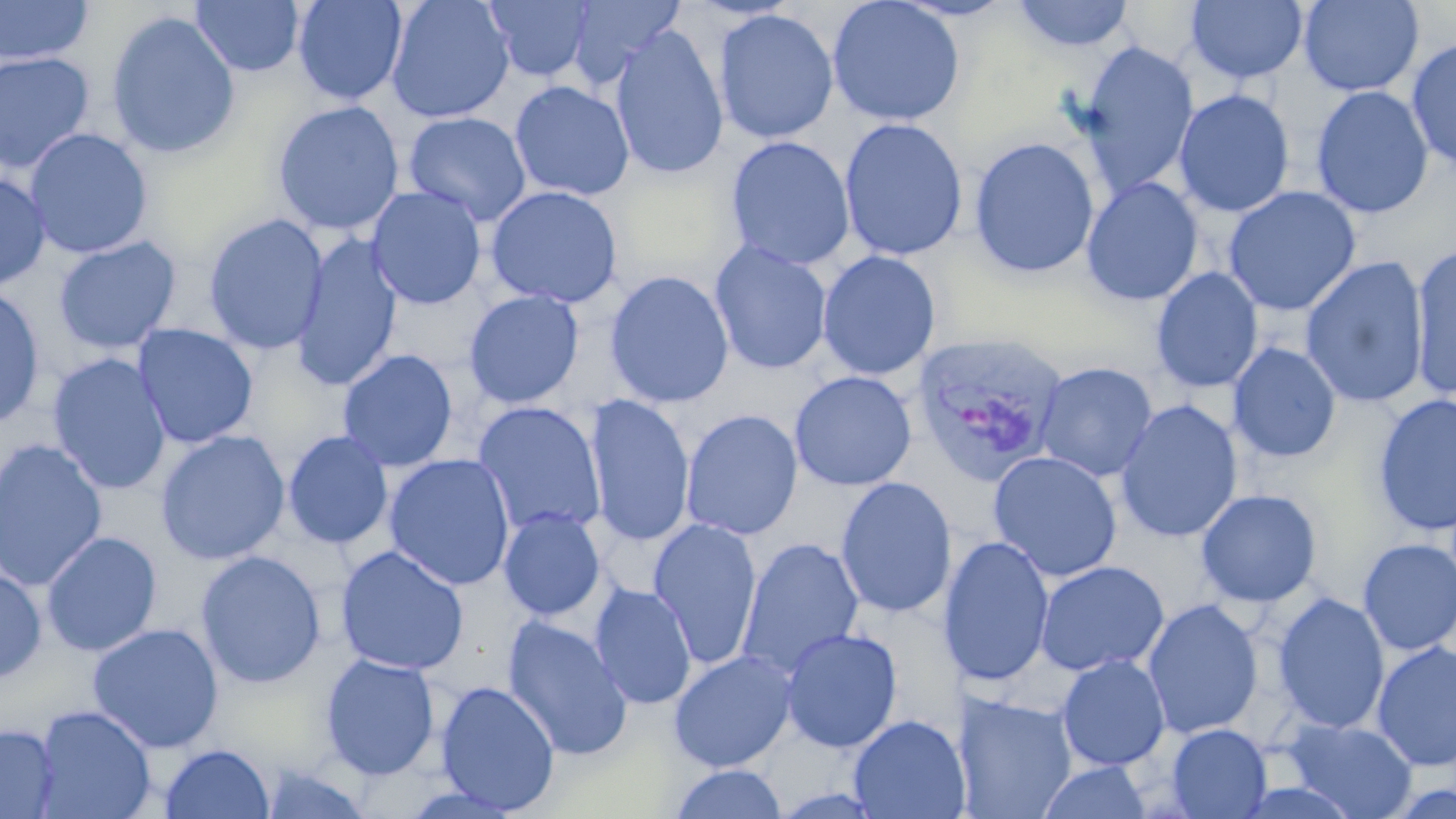
{
  "slide_level_diagnosis": "Plasmodium vivax",
  "image_size": "1456×819 pixels",
  "magnification": "1000x",
  "stain": "May-Grünwald-Giemsa",
  "plasmodium_vivax_infected_red_blood_cell_locations": "approximate bounding boxes as (x1,y1)-(x2,y2) corner pairs in pixels: (910,332)-(1070,488)",
  "modality": "optical microscopy",
  "field_of_view": "single",
  "preparation": "thin blood film",
  "uninfected_red_blood_cell_locations": "approximate bounding boxes as (x1,y1)-(x2,y2) corner pairs in pixels: (0,0)-(93,65), (190,0)-(305,77), (293,0)-(408,105), (385,0)-(515,124), (483,0)-(595,83), (566,0)-(686,87), (826,0)-(966,127), (1010,0)-(1136,53), (1185,0)-(1309,84), (1298,0)-(1424,97), (714,9)-(839,144), (106,10)-(241,160), (609,25)-(729,180), (1405,35)-(1456,173), (1078,42)-(1198,196), (0,51)-(96,173), (509,80)-(635,202), (1310,85)-(1433,219), (1174,89)-(1294,217), (272,100)-(405,236), (403,112)-(532,226), (839,118)-(968,262), (25,128)-(153,259), (725,136)-(855,271), (969,137)-(1100,278), (0,171)-(51,292), (1081,177)-(1203,306), (366,185)-(487,310), (485,185)-(623,308), (1223,185)-(1361,316), (203,213)-(328,355), (290,234)-(404,393), (53,236)-(182,355), (709,240)-(833,375), (1410,243)-(1456,400), (817,250)-(941,381), (1300,256)-(1429,408), (1150,267)-(1263,394), (604,270)-(735,409), (0,284)-(45,430), (463,289)-(584,409), (132,324)-(259,448), (1228,343)-(1342,464), (337,349)-(458,472), (47,353)-(172,496), (1034,362)-(1158,482), (789,371)-(917,491), (584,394)-(695,548), (1372,394)-(1456,537), (1114,400)-(1243,543), (472,401)-(606,538), (681,409)-(803,541), (154,430)-(290,565), (282,430)-(393,550), (0,438)-(108,592), (987,451)-(1123,582), (383,453)-(516,592), (835,477)-(958,619), (1195,489)-(1322,608), (498,507)-(606,621), (647,519)-(763,669), (41,531)-(162,657), (939,535)-(1055,687), (737,538)-(865,679), (1357,538)-(1456,655), (335,545)-(469,675), (194,550)-(327,690), (1035,560)-(1169,677), (0,565)-(47,684), (590,583)-(697,710), (1272,592)-(1390,735), (1142,599)-(1264,739), (503,615)-(632,760), (87,623)-(224,753), (780,627)-(903,753), (1371,640)-(1456,772), (668,649)-(797,772), (319,653)-(441,780), (1057,654)-(1170,771), (435,680)-(560,814), (956,692)-(1077,818), (33,705)-(156,819), (848,714)-(970,819), (1283,718)-(1417,818), (0,724)-(59,818), (1166,724)-(1272,818), (159,743)-(275,818), (1036,761)-(1154,819), (259,762)-(374,819), (668,764)-(789,819)"
}